Locate every Plasmodium falciparum-infected red blood cell.
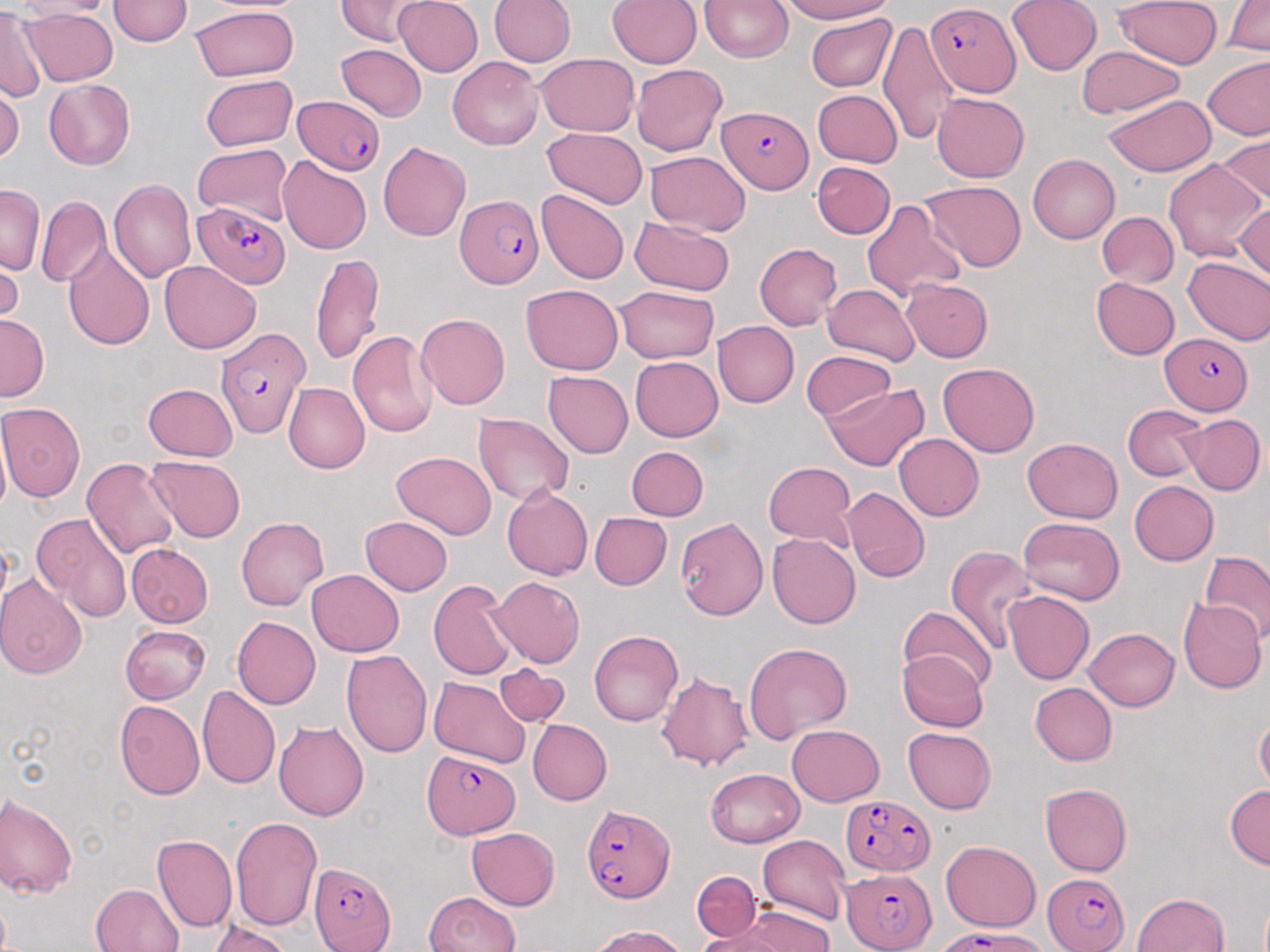
Approximate bounding boxes as named x1/y1/x2/y2 corners in pixels.
Plasmodium falciparum-infected red blood cells: (x1=929, y1=3, x2=1022, y2=93), (x1=295, y1=97, x2=384, y2=176), (x1=718, y1=107, x2=814, y2=194), (x1=457, y1=195, x2=546, y2=288), (x1=193, y1=202, x2=292, y2=290), (x1=216, y1=326, x2=310, y2=435), (x1=1159, y1=334, x2=1252, y2=414), (x1=421, y1=751, x2=519, y2=836), (x1=839, y1=794, x2=934, y2=875), (x1=581, y1=804, x2=673, y2=905), (x1=311, y1=860, x2=394, y2=952), (x1=844, y1=866, x2=935, y2=951), (x1=1041, y1=869, x2=1131, y2=952), (x1=949, y1=931, x2=1052, y2=952).

Summary:
  - Uninfected red blood cell locations: (x1=109, y1=0, x2=192, y2=47), (x1=332, y1=0, x2=428, y2=44), (x1=392, y1=0, x2=483, y2=75), (x1=488, y1=0, x2=574, y2=70), (x1=607, y1=0, x2=702, y2=69), (x1=776, y1=0, x2=897, y2=23), (x1=1009, y1=0, x2=1102, y2=76), (x1=1115, y1=0, x2=1220, y2=70), (x1=1222, y1=0, x2=1270, y2=56), (x1=701, y1=1, x2=793, y2=63), (x1=191, y1=6, x2=298, y2=81), (x1=0, y1=7, x2=42, y2=104), (x1=24, y1=7, x2=118, y2=85), (x1=806, y1=16, x2=895, y2=92), (x1=878, y1=17, x2=955, y2=149), (x1=336, y1=43, x2=426, y2=121), (x1=1075, y1=47, x2=1186, y2=118), (x1=537, y1=53, x2=641, y2=138), (x1=449, y1=58, x2=545, y2=150), (x1=1200, y1=59, x2=1270, y2=142), (x1=632, y1=65, x2=728, y2=155), (x1=198, y1=74, x2=298, y2=149), (x1=44, y1=79, x2=136, y2=170), (x1=0, y1=88, x2=23, y2=167), (x1=812, y1=88, x2=902, y2=168), (x1=932, y1=94, x2=1029, y2=182), (x1=1105, y1=94, x2=1216, y2=176), (x1=542, y1=129, x2=647, y2=209), (x1=1214, y1=133, x2=1269, y2=209), (x1=377, y1=140, x2=471, y2=240), (x1=193, y1=142, x2=293, y2=226), (x1=644, y1=153, x2=751, y2=236), (x1=1026, y1=154, x2=1120, y2=243), (x1=277, y1=155, x2=372, y2=255), (x1=1162, y1=157, x2=1265, y2=266), (x1=813, y1=163, x2=891, y2=239), (x1=108, y1=178, x2=196, y2=286), (x1=921, y1=180, x2=1027, y2=272), (x1=1, y1=188, x2=42, y2=273), (x1=534, y1=190, x2=630, y2=284), (x1=36, y1=197, x2=108, y2=289), (x1=862, y1=197, x2=963, y2=304), (x1=1236, y1=205, x2=1269, y2=285), (x1=1095, y1=210, x2=1177, y2=290), (x1=631, y1=217, x2=735, y2=295), (x1=61, y1=243, x2=154, y2=352), (x1=755, y1=243, x2=842, y2=330), (x1=311, y1=252, x2=385, y2=366), (x1=1182, y1=256, x2=1270, y2=346), (x1=163, y1=260, x2=261, y2=351), (x1=0, y1=262, x2=22, y2=321), (x1=1091, y1=276, x2=1178, y2=361), (x1=903, y1=278, x2=994, y2=363), (x1=823, y1=284, x2=918, y2=366), (x1=520, y1=285, x2=625, y2=373), (x1=615, y1=287, x2=719, y2=362), (x1=417, y1=312, x2=511, y2=410), (x1=1, y1=314, x2=47, y2=400), (x1=712, y1=318, x2=798, y2=406), (x1=347, y1=328, x2=438, y2=438), (x1=802, y1=351, x2=898, y2=425), (x1=630, y1=356, x2=724, y2=441), (x1=939, y1=362, x2=1039, y2=458), (x1=543, y1=371, x2=634, y2=457), (x1=141, y1=383, x2=237, y2=462), (x1=282, y1=383, x2=367, y2=474), (x1=823, y1=384, x2=931, y2=471), (x1=1, y1=401, x2=86, y2=503), (x1=1123, y1=402, x2=1209, y2=481), (x1=473, y1=413, x2=576, y2=507), (x1=1179, y1=413, x2=1263, y2=494), (x1=895, y1=435, x2=985, y2=520), (x1=1022, y1=437, x2=1123, y2=522), (x1=627, y1=446, x2=708, y2=519), (x1=390, y1=453, x2=498, y2=539), (x1=144, y1=456, x2=247, y2=542), (x1=80, y1=457, x2=182, y2=560), (x1=762, y1=460, x2=857, y2=546), (x1=1130, y1=482, x2=1218, y2=564), (x1=501, y1=486, x2=592, y2=579), (x1=842, y1=488, x2=928, y2=581), (x1=590, y1=511, x2=672, y2=590), (x1=31, y1=512, x2=133, y2=622), (x1=675, y1=515, x2=767, y2=619), (x1=235, y1=516, x2=329, y2=611), (x1=359, y1=516, x2=452, y2=595), (x1=1016, y1=518, x2=1125, y2=604), (x1=768, y1=535, x2=861, y2=628), (x1=125, y1=543, x2=212, y2=628), (x1=944, y1=543, x2=1040, y2=652), (x1=1198, y1=549, x2=1270, y2=642), (x1=306, y1=567, x2=405, y2=657), (x1=0, y1=575, x2=88, y2=681), (x1=489, y1=576, x2=586, y2=666), (x1=429, y1=580, x2=518, y2=683), (x1=1003, y1=591, x2=1093, y2=685), (x1=1180, y1=595, x2=1267, y2=692), (x1=899, y1=608, x2=995, y2=693), (x1=231, y1=617, x2=320, y2=710), (x1=120, y1=621, x2=212, y2=702), (x1=1085, y1=627, x2=1180, y2=711), (x1=588, y1=628, x2=684, y2=725), (x1=743, y1=643, x2=853, y2=741), (x1=341, y1=647, x2=434, y2=760), (x1=898, y1=649, x2=988, y2=732), (x1=454, y1=659, x2=573, y2=753), (x1=494, y1=665, x2=569, y2=725), (x1=656, y1=670, x2=752, y2=772), (x1=429, y1=676, x2=530, y2=768), (x1=1028, y1=681, x2=1117, y2=765), (x1=199, y1=685, x2=282, y2=788), (x1=115, y1=701, x2=204, y2=800), (x1=1256, y1=716, x2=1269, y2=796), (x1=275, y1=717, x2=370, y2=823), (x1=528, y1=719, x2=611, y2=806), (x1=787, y1=724, x2=885, y2=805), (x1=902, y1=728, x2=997, y2=813), (x1=703, y1=761, x2=795, y2=922), (x1=707, y1=766, x2=805, y2=845), (x1=1040, y1=782, x2=1133, y2=875), (x1=1224, y1=785, x2=1269, y2=869), (x1=0, y1=793, x2=76, y2=898), (x1=230, y1=816, x2=323, y2=929), (x1=466, y1=827, x2=561, y2=911), (x1=153, y1=835, x2=237, y2=934), (x1=756, y1=835, x2=851, y2=924), (x1=941, y1=841, x2=1040, y2=933), (x1=693, y1=871, x2=760, y2=940), (x1=89, y1=883, x2=186, y2=952), (x1=424, y1=891, x2=520, y2=952), (x1=1131, y1=891, x2=1232, y2=952), (x1=712, y1=907, x2=837, y2=952), (x1=208, y1=919, x2=292, y2=952), (x1=582, y1=921, x2=697, y2=952)
  - Slide-level diagnosis: Plasmodium falciparum
  - Preparation: thin blood film
  - Modality: light microscopy
  - Image size: 1270×952 pixels
  - Magnification: 1000x
  - Stain: May-Grünwald-Giemsa
  - Field of view: one of a larger specimen